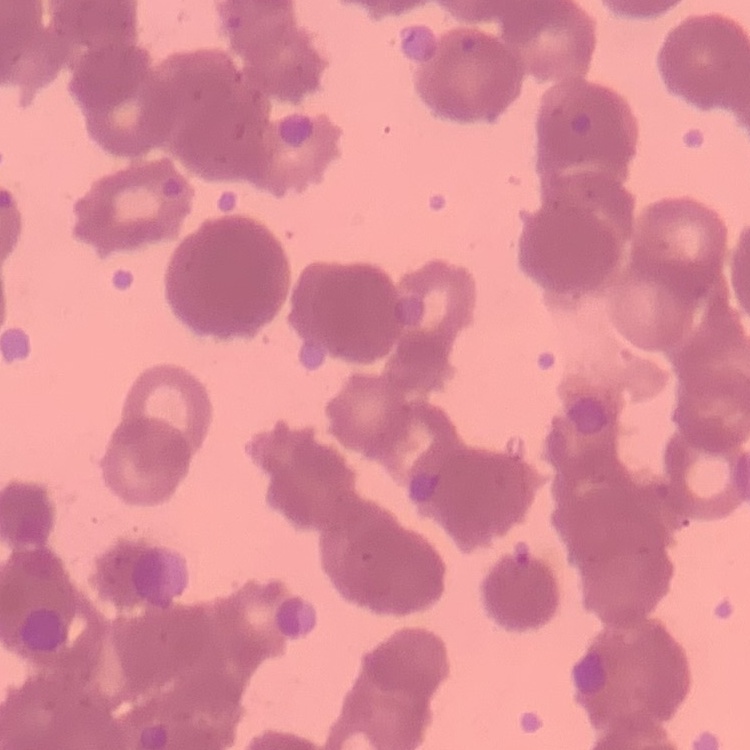
The red blood cells exhibit rouleaux formation. Field's or Giemsa stain. Thin peripheral smear. One tile cut from a larger photomicrograph.